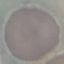

Summary:
  - Result: negative for malaria parasites
  - Stain: Giemsa
  - Preparation: thin smear
  - Capture: smartphone camera at the microscope eyepiece
  - Image type: cell patch, automatically extracted from a larger field of view and resized to 64 × 64 pixels